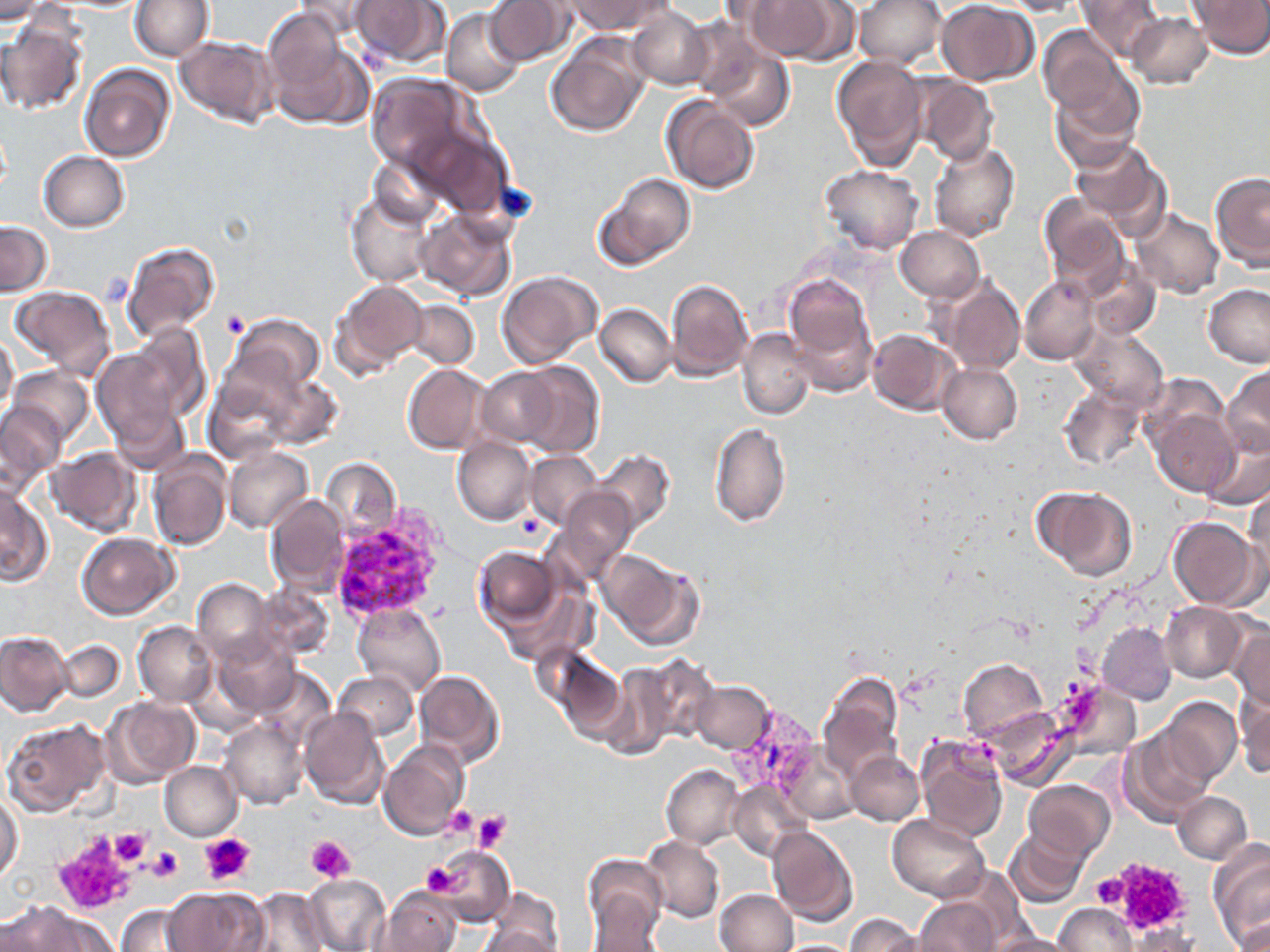
slide-level diagnosis = Plasmodium vivax
field of view = single
Plasmodium vivax-infected red blood cell locations = approximate bounding boxes as (x1, y1, x2, y2) in pixels: (728, 706, 823, 807)
modality = optical microscopy
preparation = thin blood smear
platelet locations = approximate bounding boxes as (x1, y1, x2, y2) in pixels: (220, 309, 250, 337), (513, 513, 544, 540), (442, 806, 478, 840), (452, 806, 505, 845), (472, 810, 511, 854), (90, 827, 153, 888), (110, 829, 151, 867), (53, 831, 142, 915), (199, 832, 256, 886), (307, 835, 354, 883), (146, 845, 183, 882), (1106, 857, 1194, 937), (422, 861, 464, 896), (1090, 874, 1128, 907)
image size = 1270×952 pixels
stain = May-Grünwald-Giemsa
magnification = 1000x
uninfected red blood cell locations = approximate bounding boxes as (x1, y1, x2, y2) in pixels: (0, 0, 50, 22), (131, 0, 212, 60), (295, 0, 380, 42), (347, 0, 449, 68), (485, 0, 575, 67), (566, 0, 670, 36), (740, 0, 841, 60), (854, 0, 945, 69), (997, 0, 1087, 16), (1075, 0, 1164, 61), (1193, 0, 1270, 58), (935, 1, 1039, 85), (626, 7, 712, 89), (442, 8, 526, 96), (1127, 12, 1214, 89), (0, 17, 88, 115), (1038, 24, 1128, 117), (266, 26, 373, 129), (175, 35, 279, 128), (545, 36, 649, 138), (700, 40, 796, 132), (832, 56, 928, 166), (79, 63, 175, 162), (1049, 71, 1144, 168), (365, 74, 478, 178), (913, 76, 999, 165), (660, 94, 758, 194), (408, 123, 511, 219), (1069, 139, 1171, 237), (928, 141, 1020, 243), (39, 151, 130, 231), (369, 152, 451, 231), (819, 164, 922, 254), (598, 172, 695, 268), (1210, 172, 1270, 271), (346, 189, 435, 287), (1040, 196, 1129, 295), (414, 206, 517, 301), (1131, 208, 1224, 298), (1, 221, 51, 295), (896, 226, 985, 302), (120, 239, 220, 344), (1082, 259, 1163, 341), (496, 271, 602, 369), (782, 274, 876, 388), (1020, 274, 1100, 366), (940, 277, 1023, 375), (666, 278, 753, 380), (330, 280, 427, 378), (1203, 284, 1270, 368), (9, 285, 117, 380), (403, 300, 479, 369), (596, 304, 675, 387), (226, 312, 326, 400), (119, 324, 212, 424), (1071, 325, 1168, 412), (738, 327, 817, 421), (867, 329, 958, 415), (0, 331, 19, 417), (91, 341, 196, 448), (509, 361, 604, 456), (938, 362, 1022, 444), (402, 363, 491, 455), (9, 365, 94, 443), (1223, 365, 1270, 458), (477, 366, 563, 447), (246, 367, 342, 451), (203, 368, 304, 465), (1142, 372, 1231, 454), (1058, 382, 1148, 470), (0, 401, 64, 487), (111, 407, 191, 474), (1151, 407, 1239, 497), (710, 421, 791, 525), (453, 436, 536, 525), (1202, 436, 1270, 510), (222, 445, 312, 533), (47, 447, 141, 537), (594, 449, 675, 533), (525, 450, 603, 528), (148, 451, 231, 551), (320, 457, 401, 539), (0, 485, 51, 586), (555, 487, 638, 580), (1036, 487, 1137, 580), (1244, 488, 1270, 583), (264, 495, 350, 592), (1167, 516, 1261, 610), (76, 533, 177, 619), (473, 545, 563, 631), (600, 552, 703, 650), (495, 575, 596, 667), (193, 578, 277, 665), (251, 583, 334, 660), (352, 602, 446, 698), (1161, 603, 1248, 683), (133, 621, 217, 707), (1095, 621, 1177, 705), (1227, 623, 1270, 710), (0, 630, 73, 716), (213, 633, 300, 720), (55, 640, 126, 701), (549, 649, 630, 741), (637, 655, 719, 745), (957, 659, 1047, 741), (595, 666, 674, 758), (253, 667, 335, 753), (413, 669, 503, 768), (332, 670, 418, 743), (819, 671, 903, 781), (690, 681, 775, 754), (1062, 681, 1141, 759), (1236, 692, 1270, 780), (103, 696, 201, 787), (1159, 696, 1242, 786), (986, 706, 1075, 789), (298, 708, 390, 811), (413, 709, 502, 811), (1, 718, 111, 818), (220, 719, 308, 810), (1120, 728, 1214, 825), (915, 736, 1008, 843), (377, 741, 468, 842), (774, 745, 857, 824), (847, 751, 924, 825), (159, 761, 241, 841), (661, 763, 745, 848), (1024, 781, 1115, 861), (728, 782, 811, 861), (1172, 792, 1251, 863), (1, 794, 24, 886), (887, 813, 989, 901), (767, 825, 858, 926), (1004, 825, 1091, 909), (640, 835, 724, 924), (1209, 843, 1269, 952), (435, 846, 514, 926), (584, 855, 668, 946), (301, 873, 391, 952), (399, 873, 492, 950), (162, 887, 266, 951), (243, 888, 331, 951), (376, 888, 462, 951), (480, 889, 564, 951), (715, 889, 798, 952), (915, 898, 1002, 952), (7, 900, 104, 951), (116, 903, 200, 951), (1054, 903, 1137, 952), (1228, 913, 1270, 952), (844, 915, 924, 952), (475, 923, 563, 952), (1127, 928, 1199, 952), (989, 932, 1078, 952), (774, 939, 858, 951)